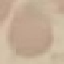
Summary:
  - Malaria status: uninfected
  - Stain: Giemsa
  - Preparation: thin smear
  - Capture: smartphone camera at the microscope eyepiece
  - Image type: automatically extracted cell patch, resized to 64 × 64 pixels